Describe the morphology of the red blood cells.
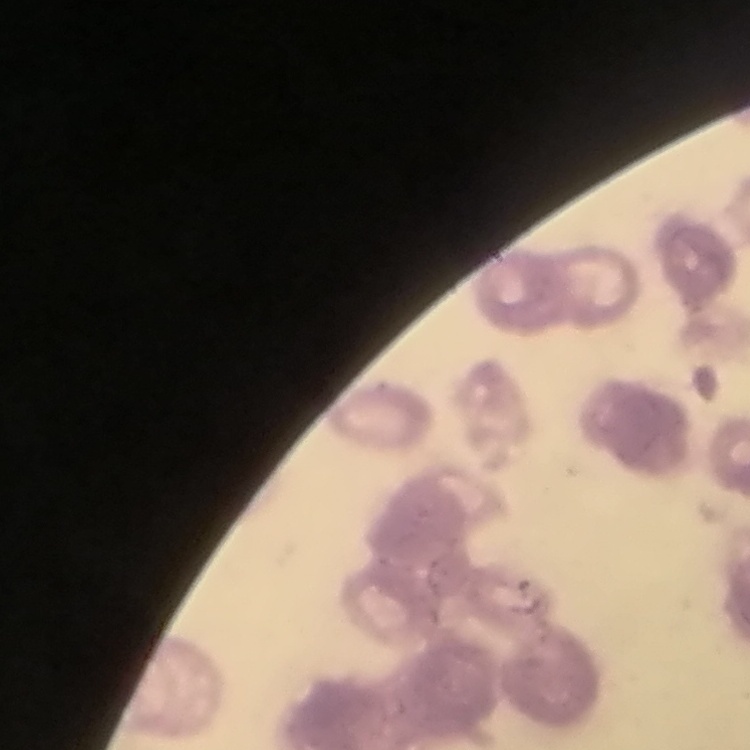
Rouleaux formation.

stain = Field's or Giemsa
preparation = thin blood film
image type = one tile cut from a larger photomicrograph